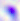
magnification = 400x
modality = photomicrograph
identification = Toxoplasma gondii